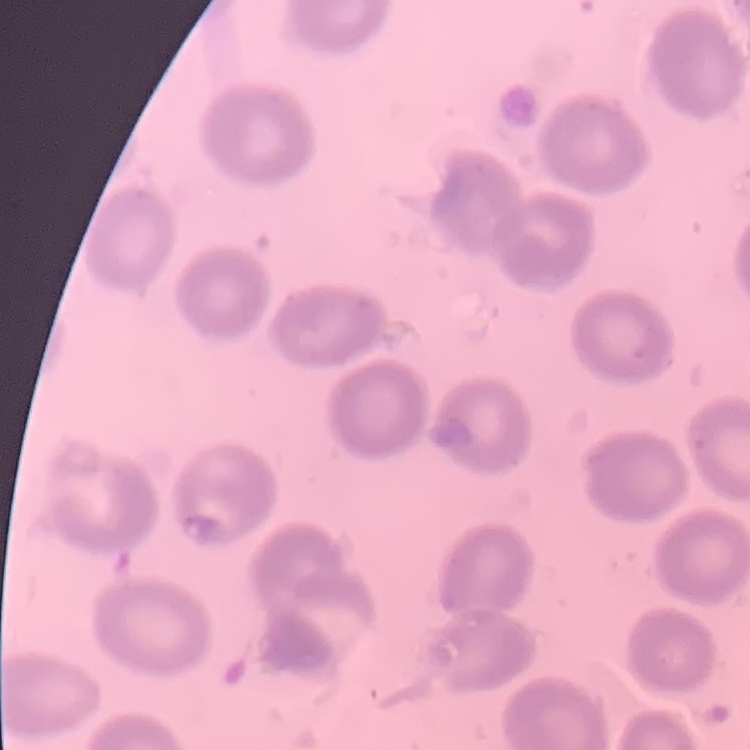

Summary:
  - Erythrocyte morphology: no rouleaux formation
  - Preparation: thin blood smear
  - Stain: Field's or Giemsa
  - Image type: one tile cut from a larger photomicrograph